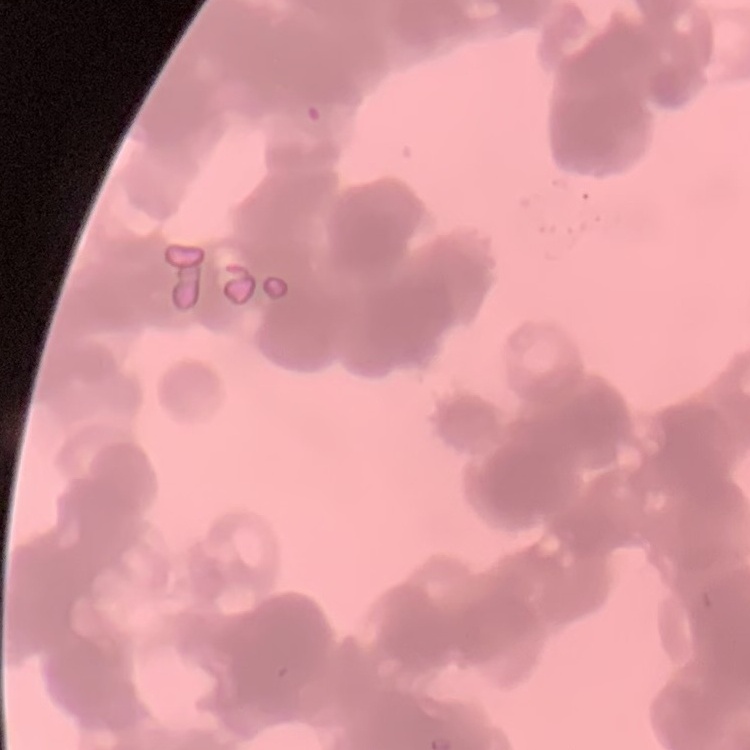

erythrocyte morphology = rouleaux formation
preparation = thin blood film
image type = one tile cut from a larger photomicrograph
stain = Field's or Giemsa